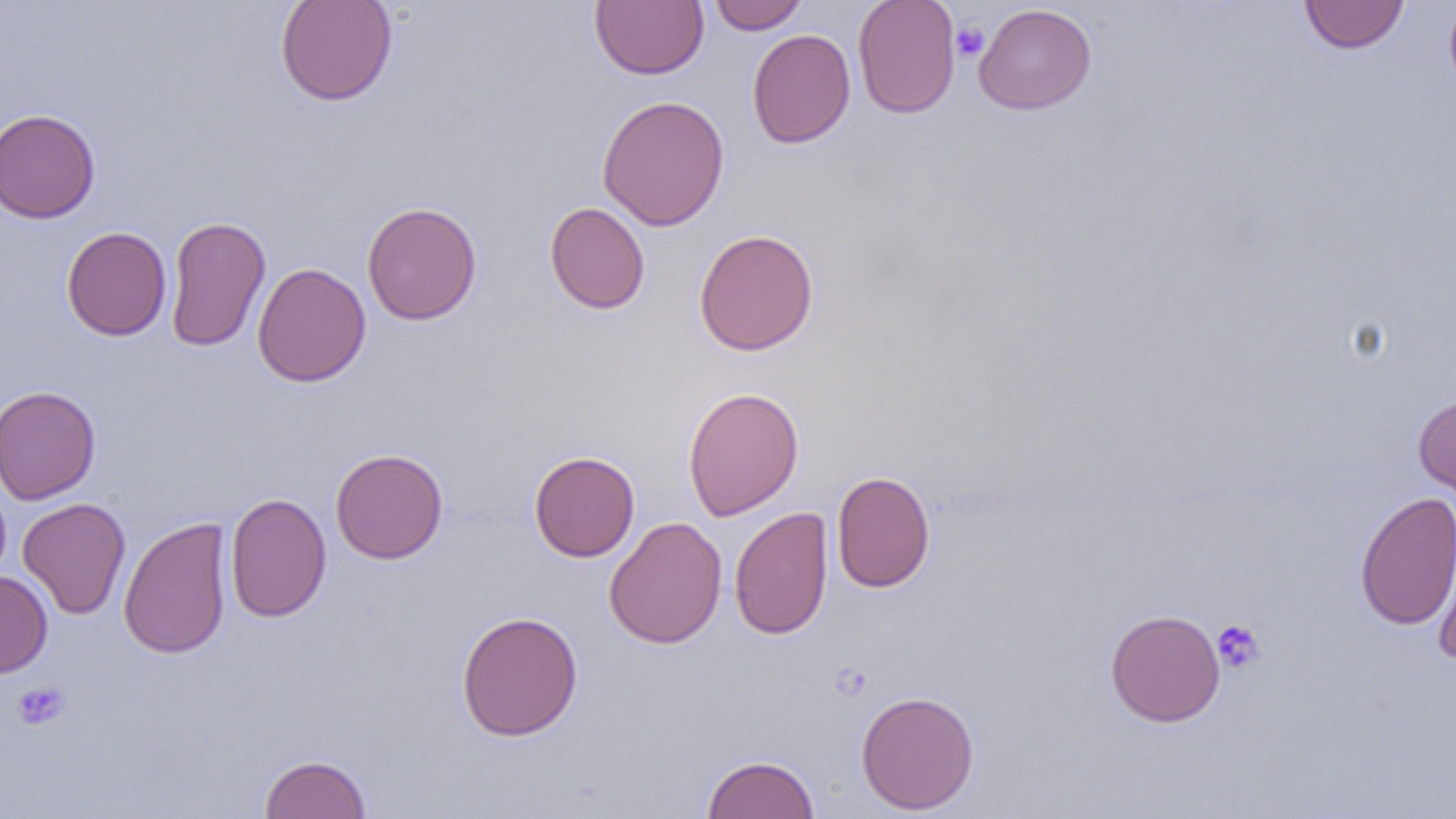
Summary:
  - Coordinate format: approximate bounding boxes as named x1/y1/x2/y2 corners in pixels
  - Platelet locations: (x1=951, y1=21, x2=989, y2=61), (x1=1212, y1=619, x2=1266, y2=674), (x1=12, y1=681, x2=70, y2=731)
  - Uninfected red blood cell locations: (x1=274, y1=0, x2=399, y2=107), (x1=709, y1=0, x2=810, y2=34), (x1=853, y1=0, x2=960, y2=119), (x1=1298, y1=0, x2=1410, y2=55), (x1=1444, y1=0, x2=1456, y2=95), (x1=591, y1=1, x2=709, y2=80), (x1=973, y1=3, x2=1097, y2=115), (x1=747, y1=28, x2=856, y2=149), (x1=597, y1=95, x2=730, y2=231), (x1=0, y1=108, x2=100, y2=223), (x1=361, y1=202, x2=483, y2=326), (x1=545, y1=202, x2=650, y2=315), (x1=164, y1=215, x2=272, y2=352), (x1=61, y1=226, x2=172, y2=341), (x1=693, y1=229, x2=819, y2=356), (x1=252, y1=262, x2=371, y2=387), (x1=0, y1=385, x2=102, y2=505), (x1=683, y1=386, x2=804, y2=520), (x1=1413, y1=393, x2=1456, y2=506), (x1=330, y1=448, x2=448, y2=564), (x1=528, y1=450, x2=640, y2=562), (x1=831, y1=470, x2=936, y2=593), (x1=1354, y1=491, x2=1456, y2=631), (x1=225, y1=493, x2=332, y2=623), (x1=17, y1=497, x2=131, y2=620), (x1=729, y1=507, x2=834, y2=640), (x1=118, y1=515, x2=233, y2=659), (x1=604, y1=516, x2=728, y2=649), (x1=1430, y1=519, x2=1456, y2=666), (x1=0, y1=571, x2=53, y2=678), (x1=1104, y1=608, x2=1225, y2=727), (x1=455, y1=610, x2=584, y2=741), (x1=856, y1=690, x2=980, y2=815), (x1=258, y1=753, x2=372, y2=818), (x1=702, y1=753, x2=820, y2=819)
  - Slide-level diagnosis: negative for blood parasites
  - Preparation: thin blood smear
  - Field of view: single
  - Modality: optical microscopy
  - Magnification: 1000x
  - Image size: 1456×819 pixels